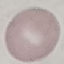

Malaria status: uninfected. Photographed with a smartphone camera at the microscope eyepiece. Thin blood smear. Automatically extracted cell patch, resized to 64 × 64 pixels. Giemsa stain.